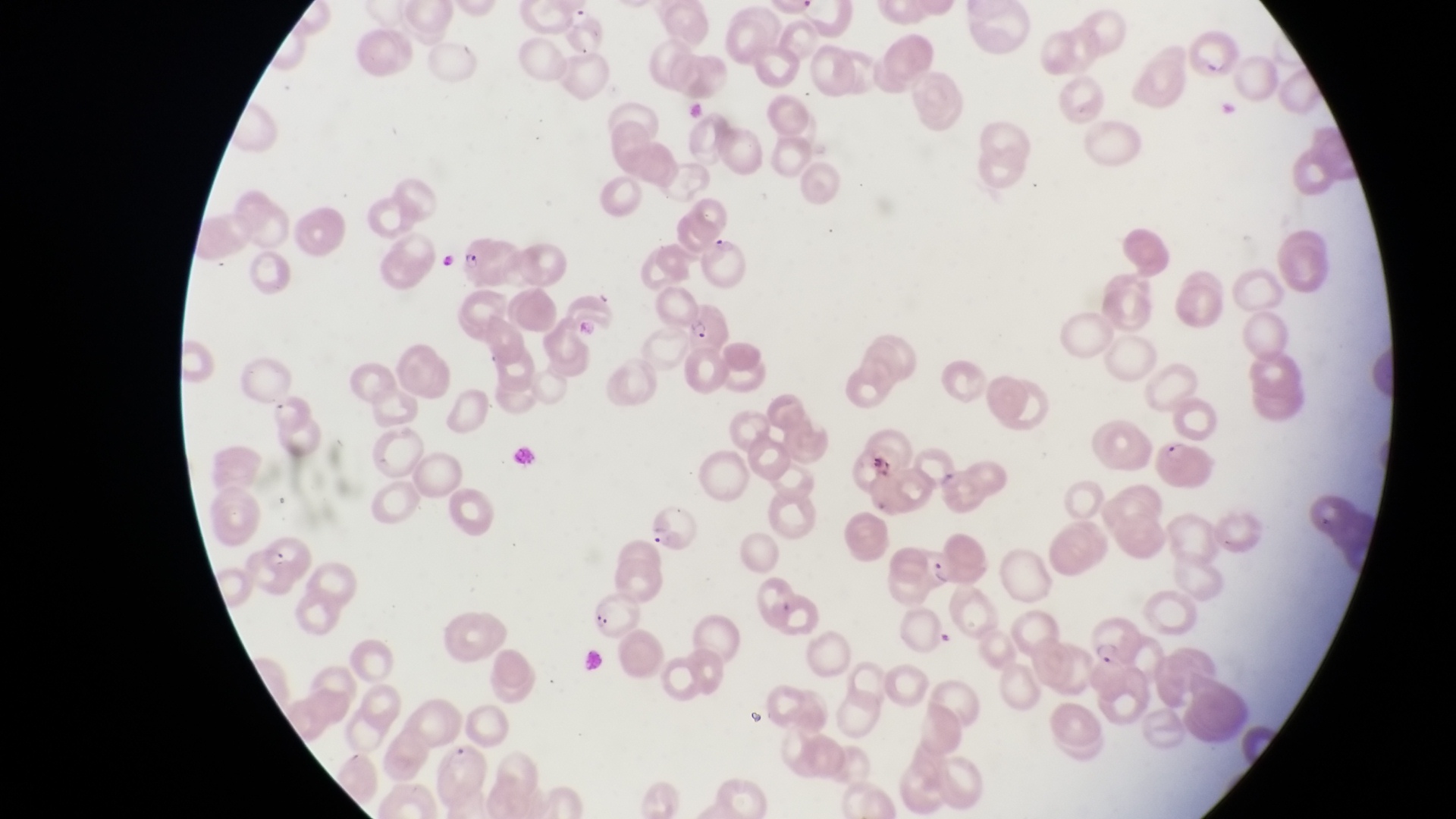
magnification = 1000x
field of view = single
parasitised red blood cell locations = approximate bounding boxes as {left, top, right, bottom} in pixels: {565, 6, 607, 59}, {1194, 32, 1243, 85}, {460, 235, 516, 293}, {563, 294, 621, 343}, {680, 301, 727, 351}, {1156, 431, 1215, 492}, {645, 497, 703, 556}, {918, 544, 955, 589}, {1093, 617, 1135, 666}
preparation = thin blood film
artifact (platelet-like body, stain precipitate, or debris) locations = approximate bounding boxes as {left, top, right, bottom} in pixels: {682, 95, 705, 124}, {872, 457, 904, 480}
image size = 1456×819 pixels
capture = smartphone photograph through the eyepiece of an Olympus CX-23 microscope
country = Uganda